Describe the morphology of the red blood cells.
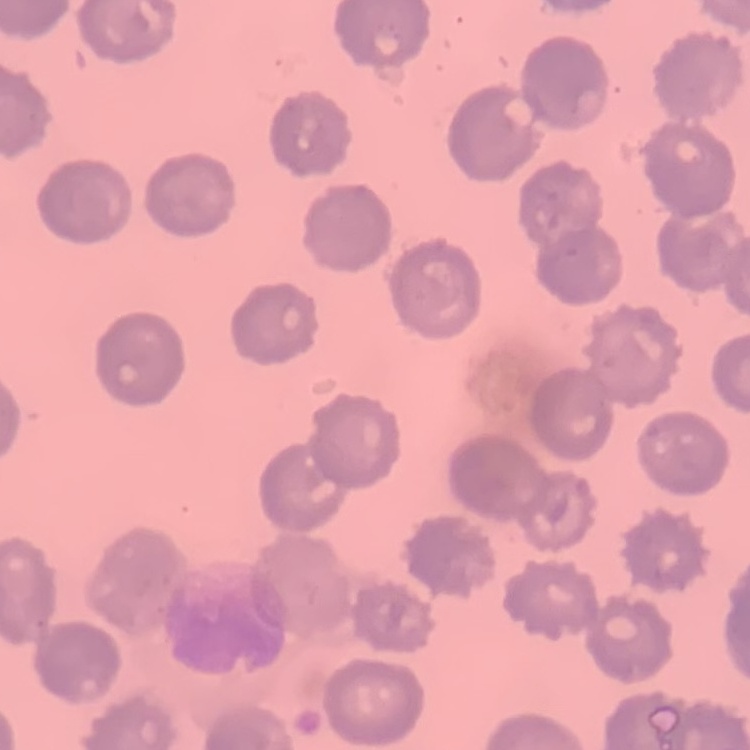

No rouleaux formation.

Stained with either Field's or Giemsa. Thin blood smear. Square crop of a larger photomicrograph.